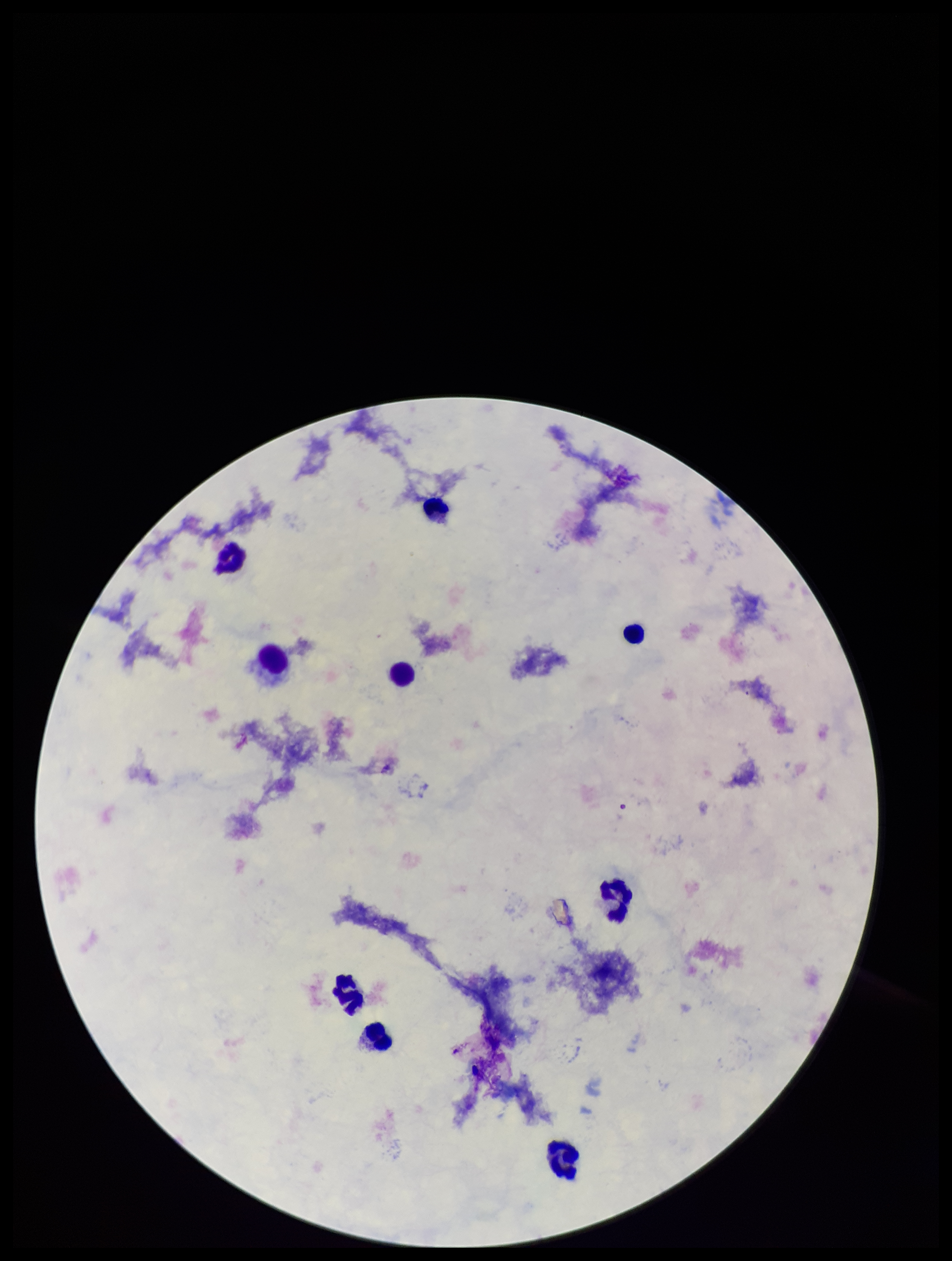
Patient malaria status: negative. Smartphone photograph taken through the eyepiece of a microscope. Preparation: thick. One field from this slide. Stained with Giemsa. Plasmodium parasites: none identified. Image is 952×1261 pixels. Leukocyte count: 9. Parasite count: 0.